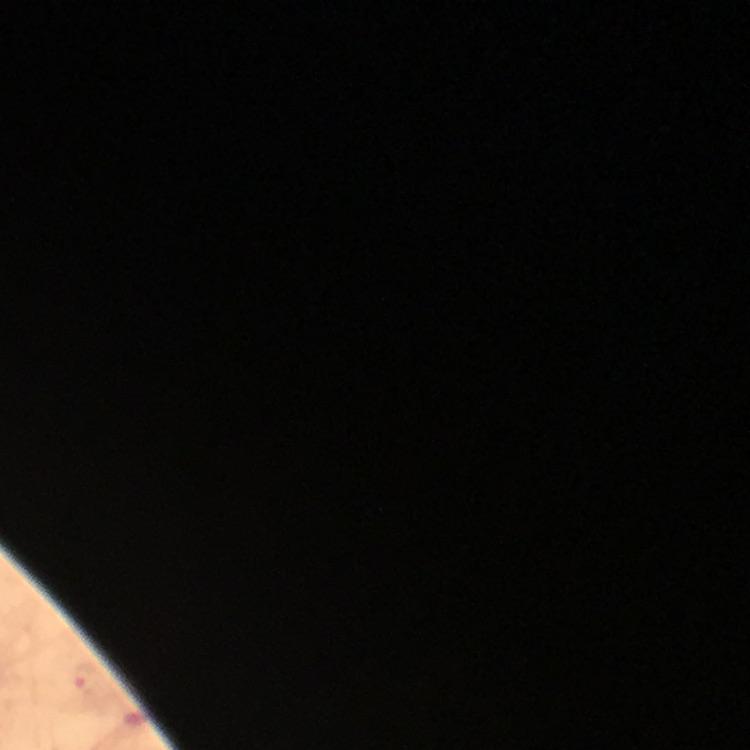

Approximate centers as [x, y] in pixels.
Summary:
  - Plasmodium parasite locations: [81, 677]
  - Stain: Giemsa
  - Preparation: thick blood film
  - Image size: 750×750 pixels
  - Context: from a diagnostic examination for malaria
  - Cropped from: a single field of view
  - Immersion oil: applied
  - Magnification: 100x
  - Capture: smartphone camera through the microscope